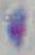
Captured at 1000x magnification. Micrograph. Toxoplasma gondii is shown.